State the blood parasite species.
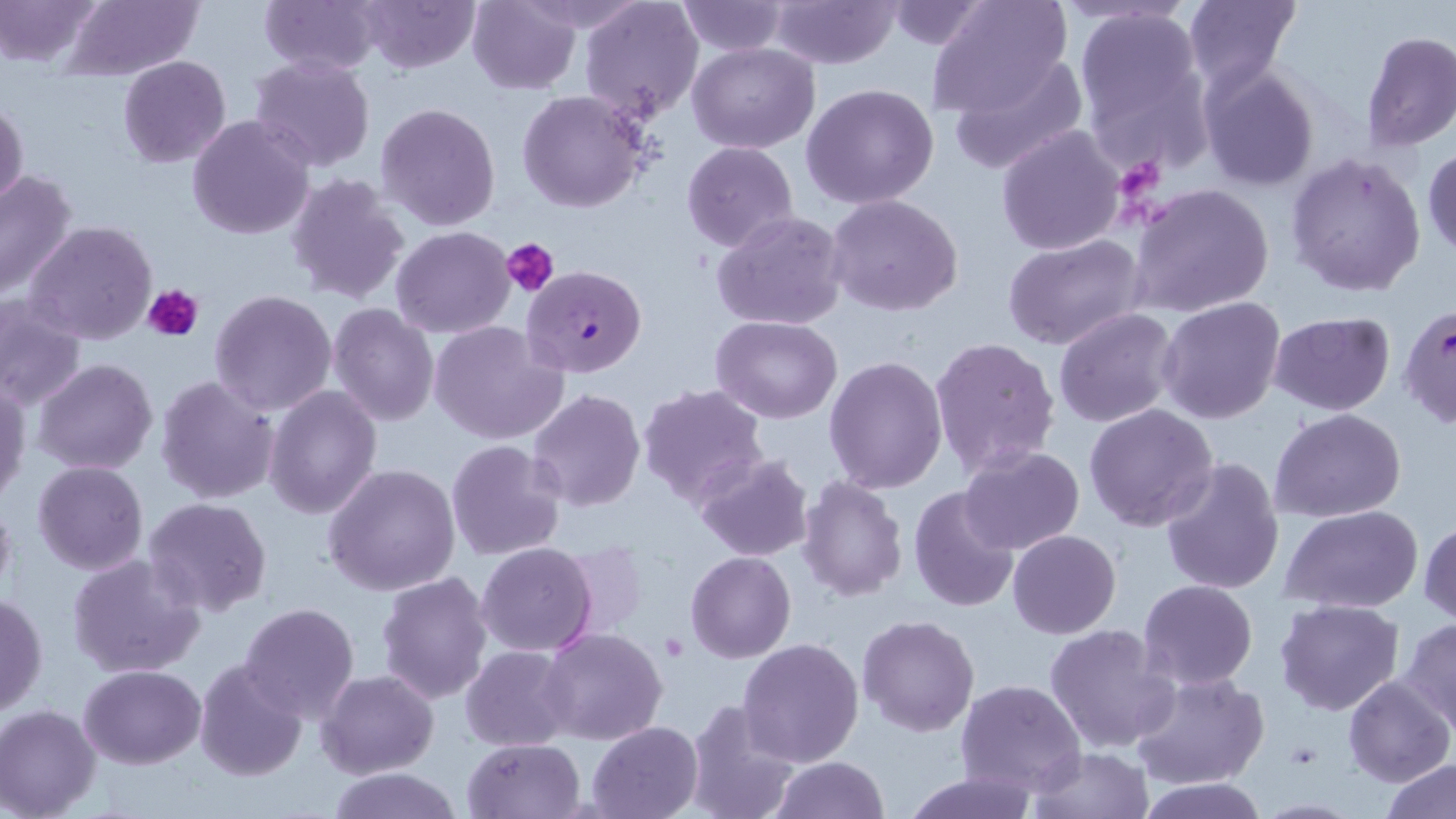

Plasmodium falciparum.

Approximate bounding boxes as [x1, y1, x2, y2] in pixels. Uninfected red blood cell locations: [2, 0, 103, 67], [260, 0, 381, 74], [356, 0, 480, 72], [579, 0, 705, 123], [765, 0, 904, 69], [883, 0, 991, 48], [1183, 0, 1299, 93], [62, 1, 204, 79], [467, 1, 581, 95], [676, 1, 788, 56], [926, 1, 1072, 118], [1073, 12, 1209, 154], [1361, 32, 1456, 151], [687, 40, 820, 152], [948, 51, 1088, 176], [118, 55, 231, 167], [249, 55, 375, 171], [1198, 65, 1321, 192], [149, 81, 281, 207], [801, 84, 941, 209], [517, 89, 652, 214], [0, 95, 27, 214], [375, 101, 502, 231], [188, 115, 313, 241], [995, 124, 1125, 255], [681, 141, 798, 253], [1423, 146, 1456, 258], [1284, 152, 1427, 297], [0, 170, 79, 301], [286, 171, 410, 304], [1131, 183, 1276, 319], [825, 193, 965, 317], [712, 210, 849, 332], [26, 219, 158, 344], [391, 225, 515, 339], [1004, 234, 1147, 351], [209, 289, 338, 417], [1, 295, 87, 411], [1158, 296, 1288, 425], [327, 302, 440, 426], [1053, 308, 1179, 428], [1269, 313, 1396, 416], [710, 315, 841, 421], [429, 319, 567, 445], [928, 336, 1060, 478], [824, 355, 948, 493], [33, 358, 159, 474], [154, 373, 280, 506], [1, 378, 30, 508], [637, 381, 769, 509], [263, 384, 381, 520], [527, 388, 647, 513], [1083, 404, 1218, 533], [1269, 408, 1407, 524], [445, 440, 567, 562], [959, 444, 1086, 555], [693, 452, 814, 562], [1161, 457, 1287, 596], [32, 461, 148, 575], [322, 461, 462, 596], [796, 476, 909, 601], [908, 484, 1022, 614], [0, 489, 16, 610], [142, 497, 272, 619], [1282, 504, 1425, 613], [1419, 519, 1456, 625], [1008, 530, 1121, 638], [477, 543, 599, 656], [686, 550, 796, 663], [67, 554, 204, 680], [374, 570, 493, 705], [1137, 579, 1258, 690], [0, 592, 47, 720], [1274, 598, 1404, 716], [238, 601, 361, 721], [858, 614, 980, 737], [1398, 617, 1456, 730], [1044, 623, 1181, 754], [538, 628, 668, 746], [737, 638, 865, 768], [460, 645, 576, 750], [193, 657, 308, 783], [78, 663, 206, 769], [1130, 669, 1269, 790], [316, 670, 437, 778], [1342, 675, 1453, 787], [955, 678, 1087, 794], [682, 699, 803, 819], [1, 705, 103, 818], [586, 721, 703, 818], [462, 738, 585, 819], [1029, 746, 1152, 819], [770, 756, 890, 818], [1381, 758, 1456, 819], [327, 767, 462, 819], [901, 769, 1040, 819], [1135, 778, 1270, 817]. Platelet locations: [1125, 162, 1176, 201], [502, 238, 560, 298], [143, 283, 205, 341]. Plasmodium falciparum-infected red blood cell locations: [523, 265, 647, 377]. Optical microscopy. Single field of view. Thin blood smear. May-Grünwald-Giemsa stain. 1000x magnification. Image is 1456×819 pixels.